Evaluate for Plasmodium parasites.
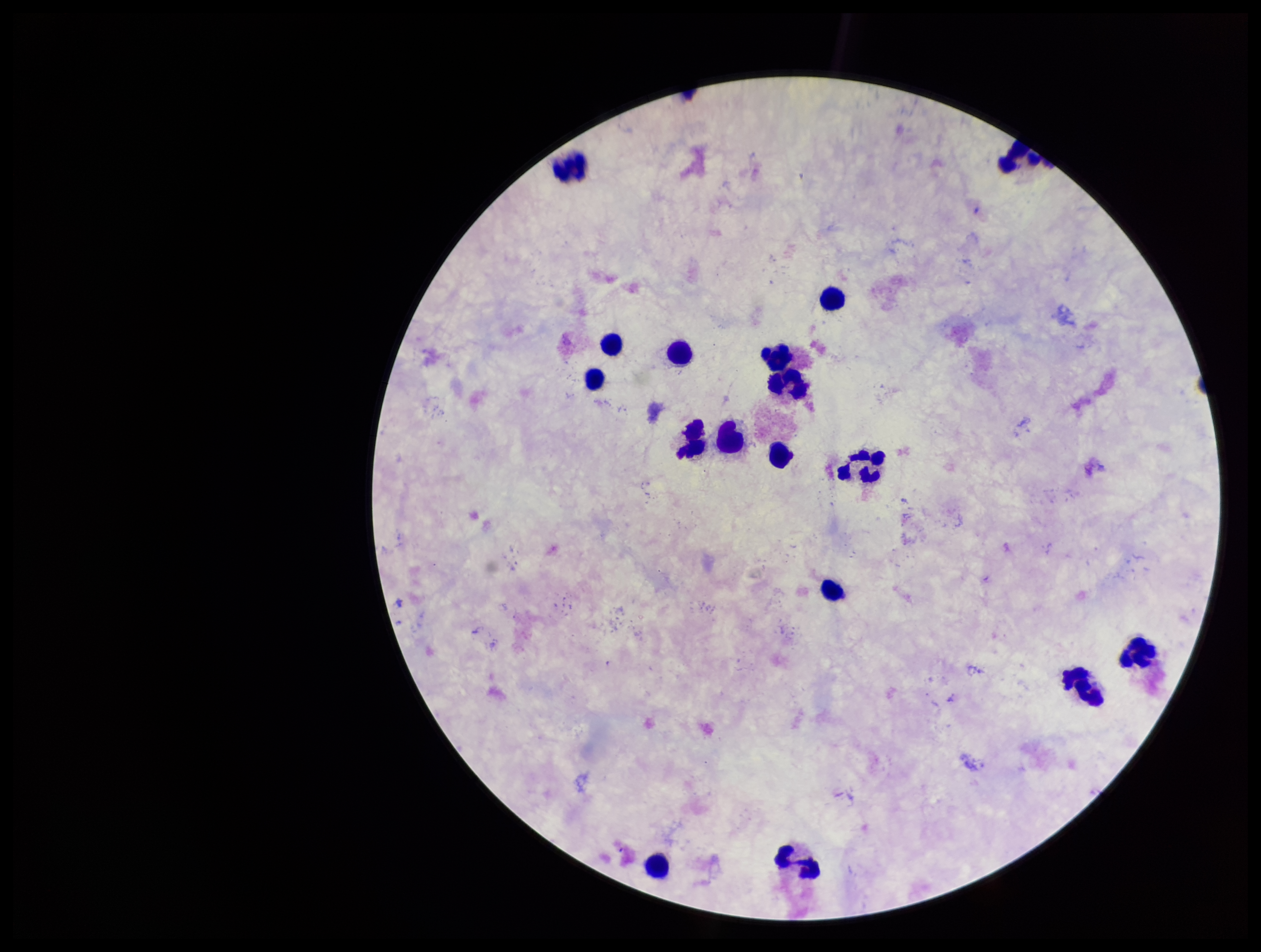

None identified.

Summary:
  - Parasite count: 0
  - Leukocyte count: 16
  - Image size: 1261×952 pixels
  - Patient malaria status: negative
  - Capture: smartphone photograph through the microscope eyepiece
  - Preparation: thick smear
  - Stain: Giemsa
  - Field of view: one from this slide